Identify the parasite.
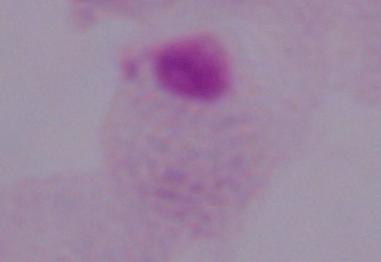
A trichomonad.

Summary:
  - Magnification: 1000x
  - Modality: micrograph